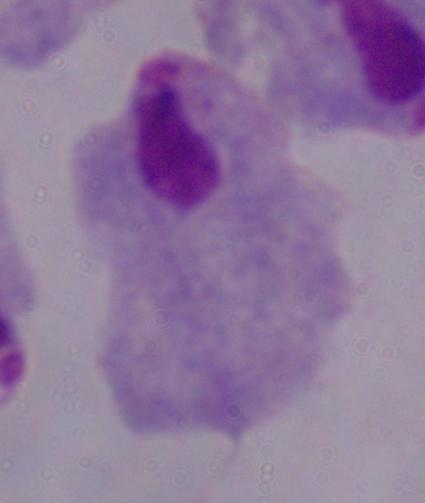

Summary:
  - Identification: trichomonad
  - Modality: micrograph
  - Magnification: 1000x